Point out every Plasmodium parasite and every leukocyte.
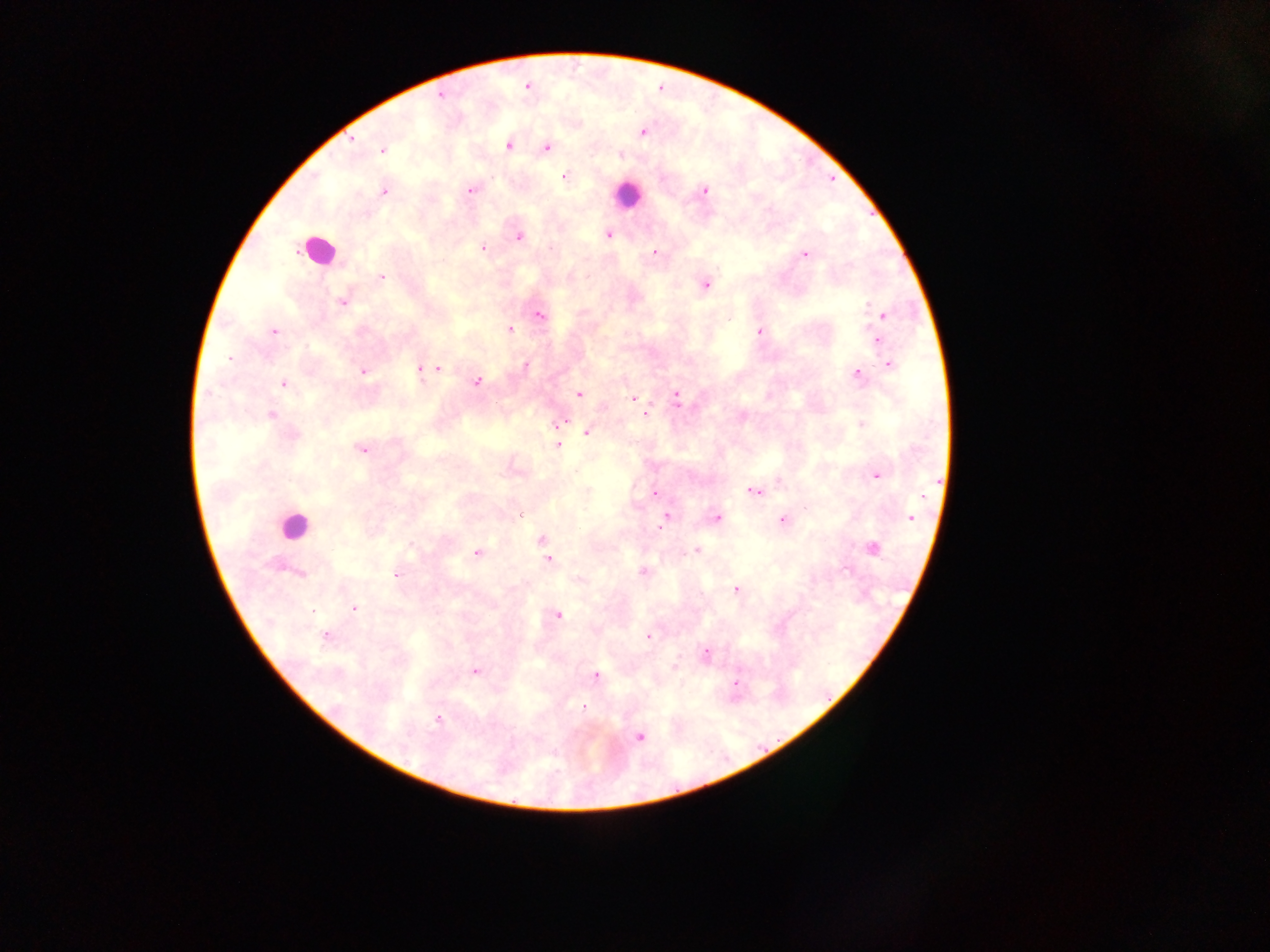
Approximate centers as x y in pixels.
Plasmodium parasites: 441 95; 642 132; 351 140; 509 146; 547 147; 381 150; 564 177; 471 191; 704 191; 383 192; 608 235; 519 237; 483 248; 655 252; 805 255; 444 260; 382 277; 705 286; 342 302; 868 305; 884 314; 539 315; 728 319; 509 329; 274 331; 759 331; 877 340; 229 358; 526 365; 888 366; 439 369; 420 370; 364 371; 856 374; 477 381; 284 383; 579 394; 677 397; 633 398; 645 413; 272 415; 561 422; 861 424; 588 432; 293 435; 557 445; 361 449; 877 476; 655 492; 755 492; 520 515; 911 517; 665 518; 717 518; 783 521; 542 540; 872 548; 696 550; 476 553; 548 559; 644 572; 300 573; 396 575; 580 580; 736 588; 354 607; 557 615; 325 637; 649 637; 706 653; 676 667; 475 671; 596 675; 736 683; 584 707; 438 719; 639 737.
Leukocytes: 626 194; 317 251; 293 525.

capture = mobile-phone photograph through a microscope
image size = 1270×952 pixels
field of view = single
country = Ghana
preparation = thick blood film